Classify this cell by malaria status.
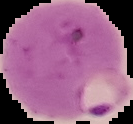

It is parasitized.

From a thin blood film. The area outside the segmented cell region is set to black. Image is 133×124 pixels.